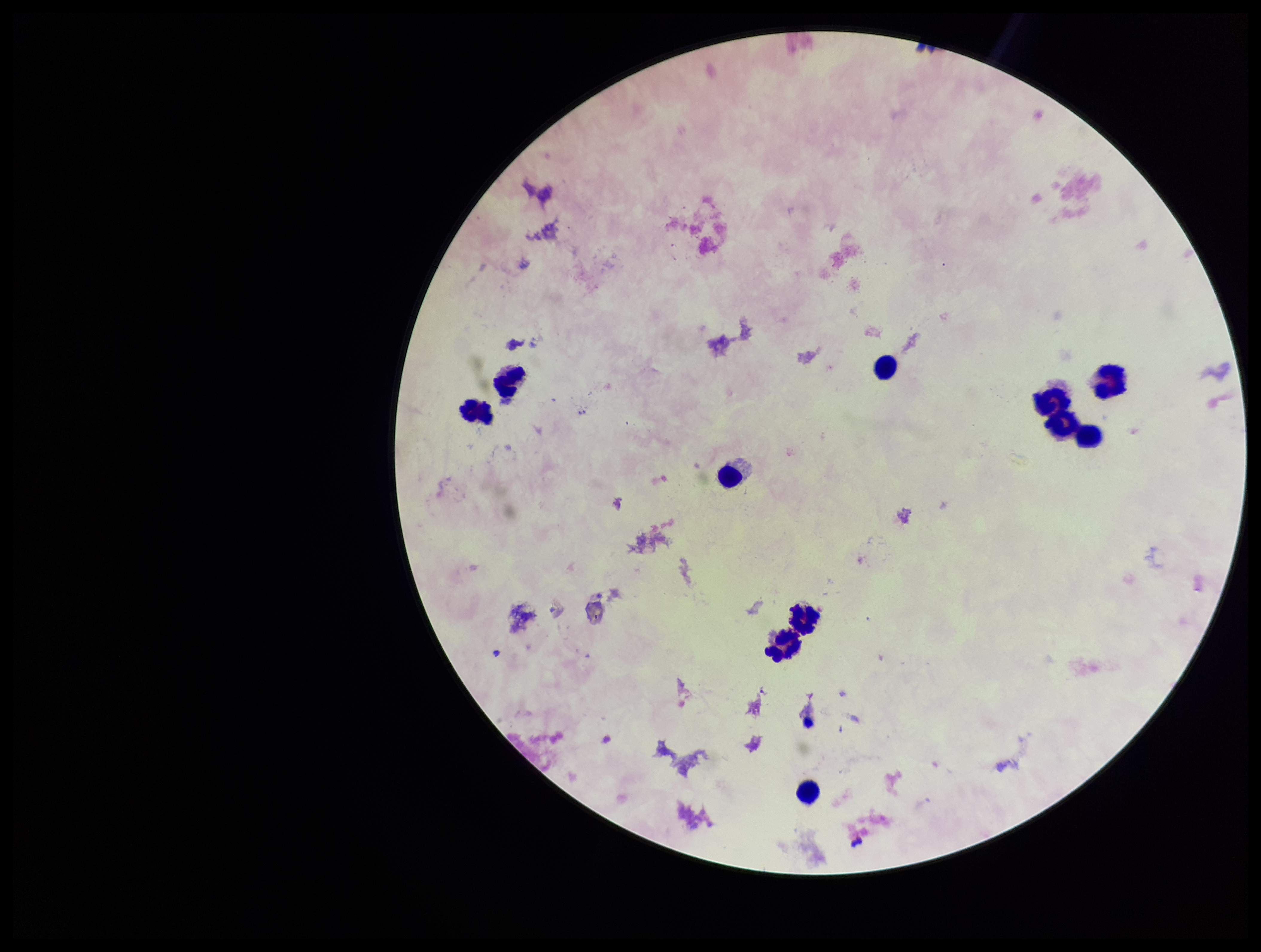
Giemsa stain. Leukocyte count: 10. Image is 1261×952 pixels. Species reported for this patient: Plasmodium falciparum. Patient malaria status: positive. Parasite count: 0. Smartphone photograph taken through the eyepiece of a microscope. Plasmodium parasites: none detected. One field from this slide. Preparation: thick smear.